Name the blood parasite species.
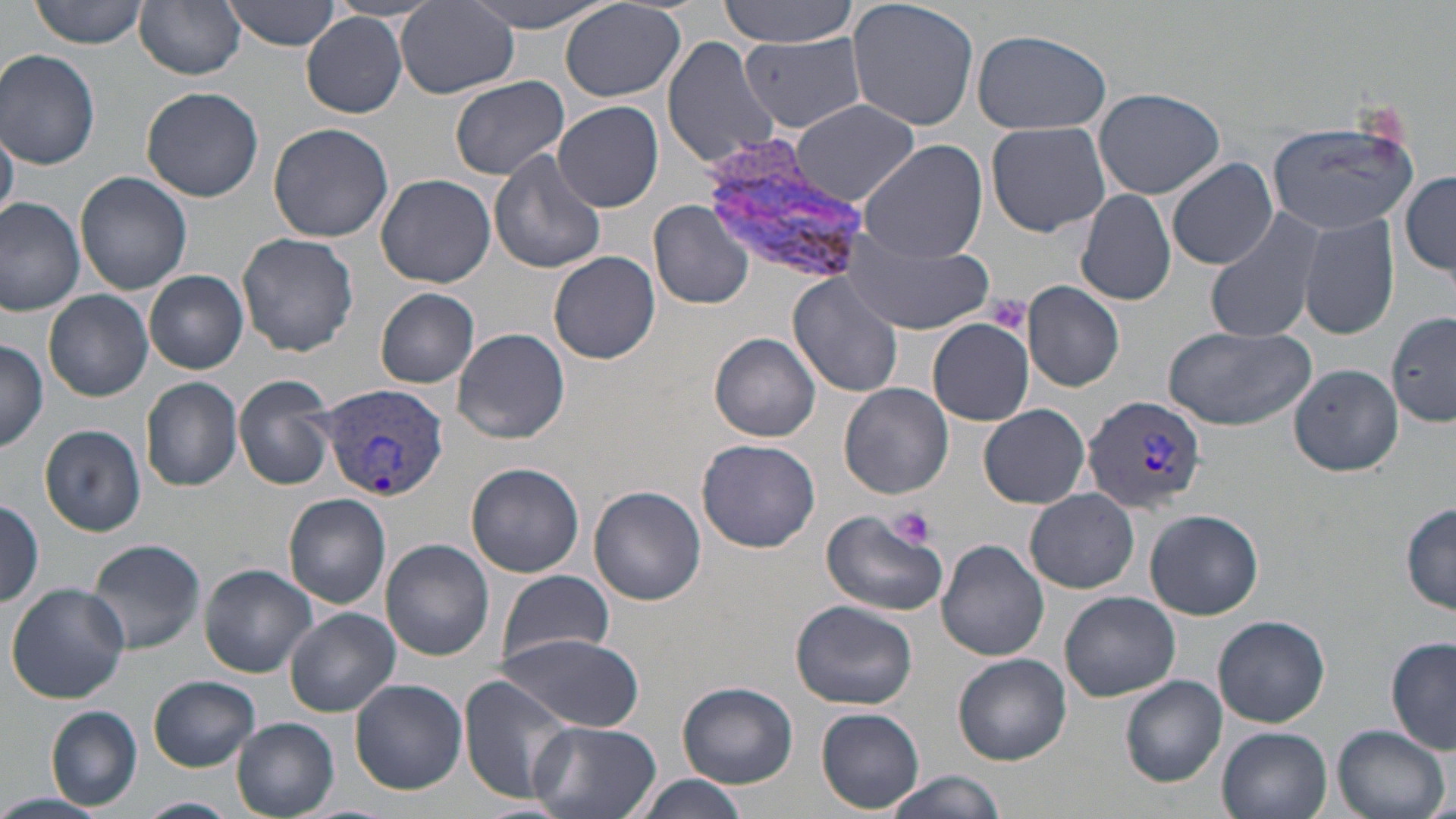
Plasmodium vivax.

Approximate bounding boxes as [x1, y1, x2, y2] in pixels. Plasmodium vivax-infected red blood cell locations: [700, 135, 874, 286], [319, 381, 451, 502], [1080, 395, 1207, 513]. Platelet locations: [984, 293, 1030, 334], [888, 508, 936, 546]. Uninfected red blood cell locations: [30, 0, 149, 48], [135, 0, 246, 80], [224, 0, 342, 50], [464, 0, 621, 32], [720, 0, 860, 47], [846, 0, 981, 131], [559, 2, 687, 103], [396, 4, 518, 99], [300, 14, 407, 117], [969, 29, 1114, 134], [737, 30, 869, 133], [662, 35, 779, 171], [0, 49, 100, 170], [448, 76, 571, 180], [142, 87, 265, 202], [1093, 87, 1224, 201], [554, 101, 663, 214], [790, 101, 919, 206], [1264, 116, 1423, 237], [987, 120, 1110, 237], [268, 123, 395, 243], [0, 124, 20, 219], [1282, 137, 1412, 329], [857, 139, 989, 262], [489, 148, 607, 274], [1168, 157, 1277, 269], [1401, 171, 1456, 277], [76, 172, 192, 296], [375, 174, 497, 288], [1076, 188, 1176, 306], [0, 194, 88, 315], [649, 200, 756, 310], [1204, 208, 1327, 343], [1299, 213, 1399, 341], [237, 232, 360, 356], [843, 234, 994, 336], [550, 250, 661, 364], [145, 270, 248, 374], [787, 270, 905, 398], [1023, 282, 1124, 392], [375, 287, 480, 388], [45, 290, 152, 401], [1388, 312, 1456, 425], [925, 318, 1033, 425], [1162, 325, 1319, 432], [452, 327, 570, 443], [710, 332, 821, 441], [0, 341, 49, 452], [1288, 364, 1403, 477], [233, 375, 337, 490], [141, 377, 243, 491], [839, 384, 954, 499], [977, 404, 1091, 507], [40, 425, 146, 537], [697, 437, 821, 552], [468, 463, 584, 577], [590, 485, 705, 605], [1026, 489, 1139, 593], [283, 493, 391, 609], [0, 500, 45, 607], [1401, 504, 1456, 614], [819, 505, 950, 619], [1145, 510, 1263, 620], [971, 514, 1075, 627], [85, 538, 207, 655], [381, 538, 494, 660], [937, 540, 1048, 660], [200, 564, 316, 676], [496, 567, 614, 671], [5, 581, 131, 703], [1059, 591, 1181, 702], [791, 600, 918, 710], [285, 608, 400, 716], [1213, 614, 1331, 728], [497, 634, 643, 731], [1386, 637, 1455, 754], [954, 653, 1071, 765], [149, 675, 260, 772], [458, 675, 579, 804], [1120, 675, 1228, 785], [349, 680, 467, 794], [677, 682, 798, 788], [47, 706, 142, 811], [817, 709, 924, 814], [232, 718, 338, 818], [528, 720, 662, 819], [1330, 723, 1451, 819], [1217, 728, 1330, 819], [881, 771, 1008, 819], [631, 774, 750, 819], [0, 792, 114, 819], [137, 795, 239, 818]. Thin blood film. May-Grünwald-Giemsa-stained preparation. Image is 1456×819 pixels. 1000x magnification. One field of a larger specimen. Optical microscopy.